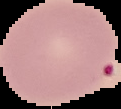

Summary:
  - Image size: 121×109 pixels
  - Image type: cell region segmented out of the field of view; surrounding area masked to black
  - Malaria status: uninfected
  - Preparation: thin blood smear